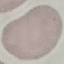

Malaria status: uninfected. Cell patch, automatically extracted from a larger field of view and resized to 64 × 64 pixels. Thin smear of blood. Acquired by smartphone through the microscope eyepiece. Giemsa-stained preparation.